Identify the blood parasite species.
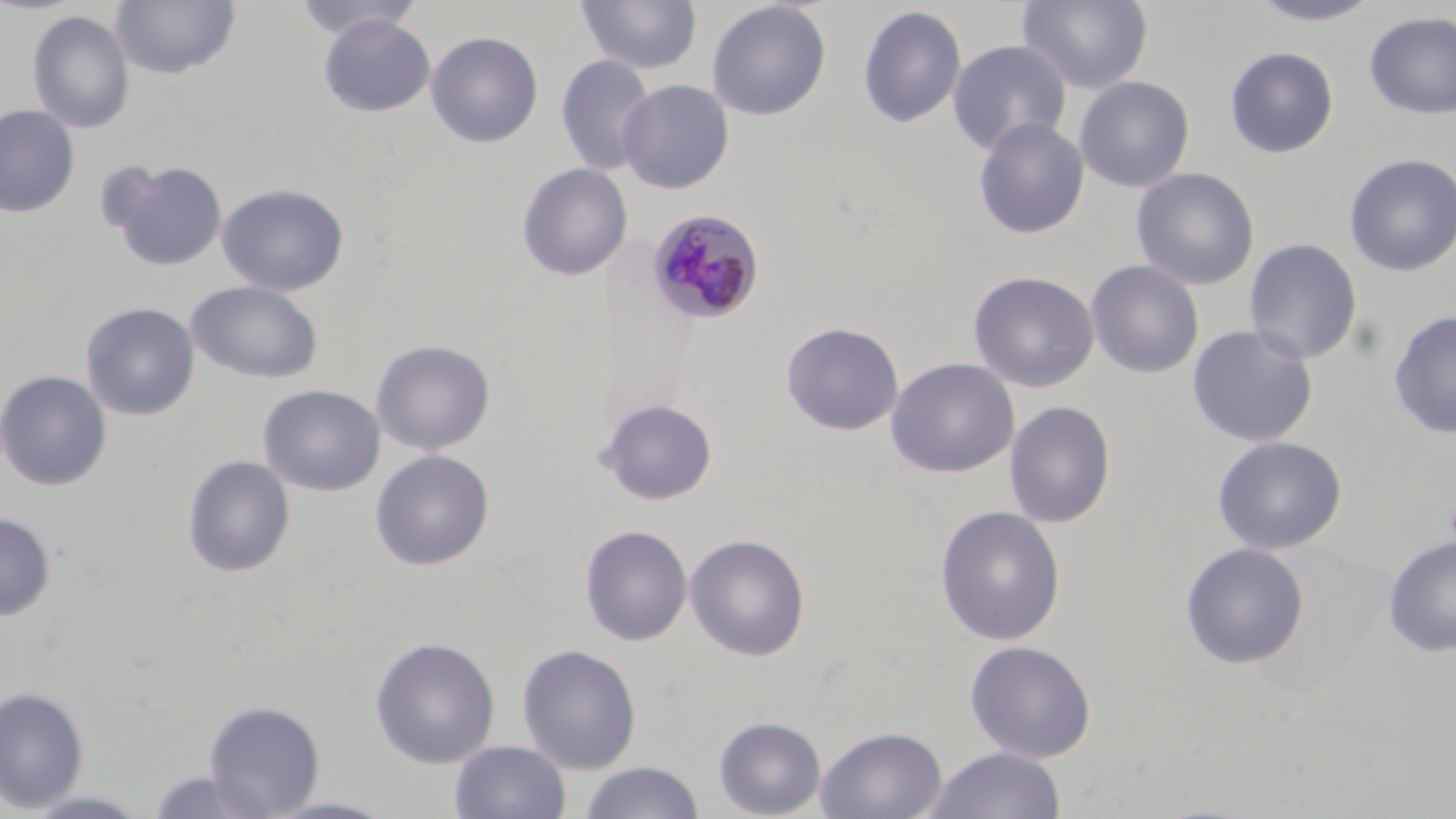

Plasmodium malariae.

Approximate bounding boxes as [x1, y1, x2, y2] in pixels. Uninfected red blood cell locations: [110, 0, 241, 81], [293, 0, 425, 41], [1018, 0, 1153, 94], [1245, 0, 1384, 26], [576, 1, 703, 75], [706, 1, 832, 120], [858, 4, 967, 129], [27, 10, 135, 134], [1363, 11, 1456, 120], [317, 14, 436, 117], [426, 30, 543, 148], [947, 39, 1072, 156], [1224, 46, 1339, 158], [556, 54, 656, 176], [1073, 76, 1195, 192], [617, 79, 734, 194], [0, 104, 80, 218], [973, 116, 1089, 238], [1343, 153, 1456, 276], [102, 158, 228, 272], [517, 163, 633, 281], [1131, 167, 1260, 291], [217, 183, 349, 296], [1243, 238, 1363, 364], [1086, 259, 1204, 378], [968, 270, 1100, 392], [186, 281, 323, 384], [81, 302, 200, 421], [1387, 309, 1456, 438], [781, 321, 904, 435], [1187, 324, 1319, 447], [371, 339, 495, 455], [885, 357, 1020, 478], [0, 369, 112, 492], [258, 384, 385, 497], [597, 398, 718, 506], [1004, 400, 1116, 528], [1212, 436, 1347, 554], [370, 449, 494, 571], [182, 454, 295, 578], [935, 505, 1066, 645], [0, 512, 56, 620], [579, 524, 693, 646], [684, 533, 810, 661], [1383, 535, 1456, 656], [1180, 542, 1310, 669], [369, 636, 501, 769], [964, 639, 1096, 763], [516, 642, 642, 773], [0, 685, 89, 813], [203, 699, 325, 817], [713, 715, 826, 818], [816, 724, 947, 819], [449, 740, 571, 819], [924, 746, 1067, 819], [577, 762, 707, 819], [146, 768, 269, 818], [21, 789, 155, 818]. Plasmodium malariae-infected red blood cell locations: [646, 208, 765, 326]. Captured at 1000x magnification. Thin blood smear. Image is 1456×819 pixels. May-Grünwald-Giemsa stain. Single field of view. Optical microscopy.